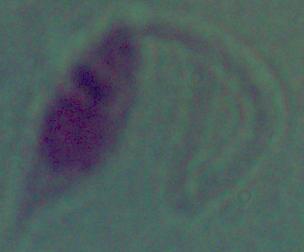
identification = Leishmania
modality = photomicrograph
magnification = 1000x